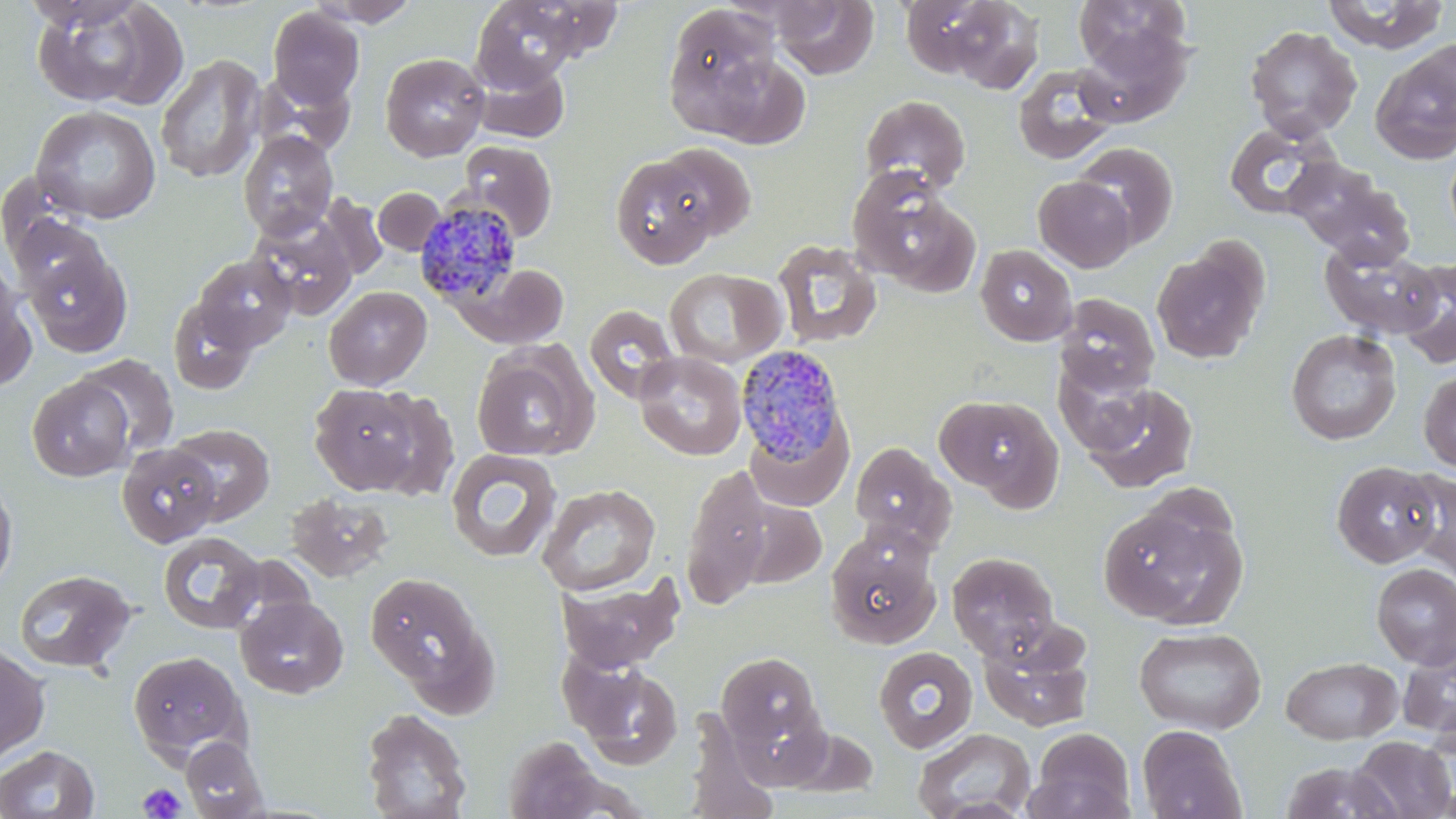

Summary:
  - Coordinate format: approximate bounding boxes as named x1/y1/x2/y2 corners in pixels
  - Uninfected red blood cell locations: (x1=27, y1=0, x2=172, y2=109), (x1=307, y1=0, x2=423, y2=27), (x1=771, y1=0, x2=878, y2=80), (x1=899, y1=0, x2=1014, y2=81), (x1=1072, y1=0, x2=1193, y2=72), (x1=1322, y1=0, x2=1450, y2=52), (x1=470, y1=1, x2=591, y2=90), (x1=939, y1=1, x2=1045, y2=94), (x1=662, y1=4, x2=786, y2=139), (x1=267, y1=6, x2=365, y2=108), (x1=1244, y1=25, x2=1363, y2=140), (x1=1075, y1=26, x2=1193, y2=127), (x1=1371, y1=46, x2=1456, y2=163), (x1=380, y1=52, x2=489, y2=161), (x1=155, y1=54, x2=265, y2=182), (x1=470, y1=58, x2=570, y2=143), (x1=1013, y1=63, x2=1120, y2=165), (x1=859, y1=95, x2=971, y2=195), (x1=31, y1=105, x2=161, y2=225), (x1=1222, y1=120, x2=1340, y2=220), (x1=238, y1=130, x2=339, y2=241), (x1=458, y1=141, x2=558, y2=241), (x1=1073, y1=142, x2=1179, y2=249), (x1=652, y1=143, x2=757, y2=243), (x1=609, y1=153, x2=723, y2=268), (x1=1286, y1=159, x2=1410, y2=261), (x1=848, y1=171, x2=978, y2=293), (x1=1034, y1=176, x2=1136, y2=272), (x1=374, y1=187, x2=445, y2=255), (x1=318, y1=194, x2=388, y2=281), (x1=250, y1=214, x2=357, y2=320), (x1=11, y1=216, x2=109, y2=303), (x1=772, y1=239, x2=883, y2=348), (x1=1319, y1=241, x2=1442, y2=340), (x1=1152, y1=242, x2=1268, y2=364), (x1=975, y1=245, x2=1077, y2=346), (x1=24, y1=247, x2=131, y2=357), (x1=192, y1=254, x2=297, y2=354), (x1=1396, y1=258, x2=1456, y2=370), (x1=463, y1=264, x2=572, y2=347), (x1=0, y1=268, x2=35, y2=391), (x1=664, y1=268, x2=786, y2=368), (x1=324, y1=286, x2=432, y2=390), (x1=1056, y1=294, x2=1160, y2=396), (x1=167, y1=296, x2=259, y2=395), (x1=584, y1=304, x2=680, y2=403), (x1=1285, y1=329, x2=1402, y2=445), (x1=471, y1=344, x2=598, y2=462), (x1=633, y1=350, x2=748, y2=460), (x1=75, y1=354, x2=179, y2=457), (x1=1055, y1=357, x2=1155, y2=456), (x1=1418, y1=370, x2=1456, y2=472), (x1=27, y1=375, x2=136, y2=482), (x1=309, y1=382, x2=422, y2=494), (x1=1083, y1=383, x2=1199, y2=493), (x1=369, y1=389, x2=460, y2=502), (x1=935, y1=394, x2=1063, y2=505), (x1=744, y1=416, x2=853, y2=512), (x1=168, y1=424, x2=276, y2=525), (x1=849, y1=441, x2=956, y2=552), (x1=117, y1=443, x2=220, y2=547), (x1=446, y1=448, x2=562, y2=562), (x1=1331, y1=460, x2=1441, y2=568), (x1=680, y1=463, x2=774, y2=609), (x1=1400, y1=470, x2=1456, y2=578), (x1=0, y1=473, x2=18, y2=595), (x1=537, y1=482, x2=661, y2=596), (x1=285, y1=492, x2=394, y2=582), (x1=737, y1=498, x2=827, y2=588), (x1=1099, y1=504, x2=1246, y2=631), (x1=824, y1=527, x2=940, y2=650), (x1=158, y1=531, x2=266, y2=635), (x1=947, y1=551, x2=1059, y2=658), (x1=1372, y1=562, x2=1456, y2=670), (x1=14, y1=568, x2=136, y2=674), (x1=363, y1=570, x2=495, y2=708), (x1=557, y1=572, x2=686, y2=673), (x1=235, y1=595, x2=348, y2=698), (x1=978, y1=626, x2=1095, y2=732), (x1=1133, y1=626, x2=1267, y2=734), (x1=1398, y1=642, x2=1456, y2=745), (x1=0, y1=644, x2=50, y2=765), (x1=873, y1=646, x2=977, y2=752), (x1=127, y1=651, x2=249, y2=764), (x1=716, y1=652, x2=823, y2=751), (x1=1280, y1=656, x2=1403, y2=744), (x1=567, y1=658, x2=684, y2=769), (x1=360, y1=707, x2=473, y2=819), (x1=682, y1=709, x2=780, y2=819), (x1=1137, y1=724, x2=1246, y2=818), (x1=779, y1=727, x2=880, y2=797), (x1=912, y1=728, x2=1036, y2=818), (x1=1028, y1=728, x2=1136, y2=819), (x1=180, y1=736, x2=269, y2=818), (x1=502, y1=736, x2=607, y2=819), (x1=1350, y1=736, x2=1455, y2=818), (x1=0, y1=744, x2=99, y2=818), (x1=1279, y1=760, x2=1402, y2=818)
  - Plasmodium malariae-infected red blood cell locations: (x1=414, y1=197, x2=523, y2=305), (x1=736, y1=343, x2=850, y2=469)
  - Platelet locations: (x1=138, y1=782, x2=189, y2=818)
  - Slide-level diagnosis: Plasmodium malariae
  - Stain: May-Grünwald-Giemsa
  - Magnification: 1000x
  - Image size: 1456×819 pixels
  - Modality: optical microscopy
  - Preparation: thin blood smear
  - Field of view: single